State the blood parasite species.
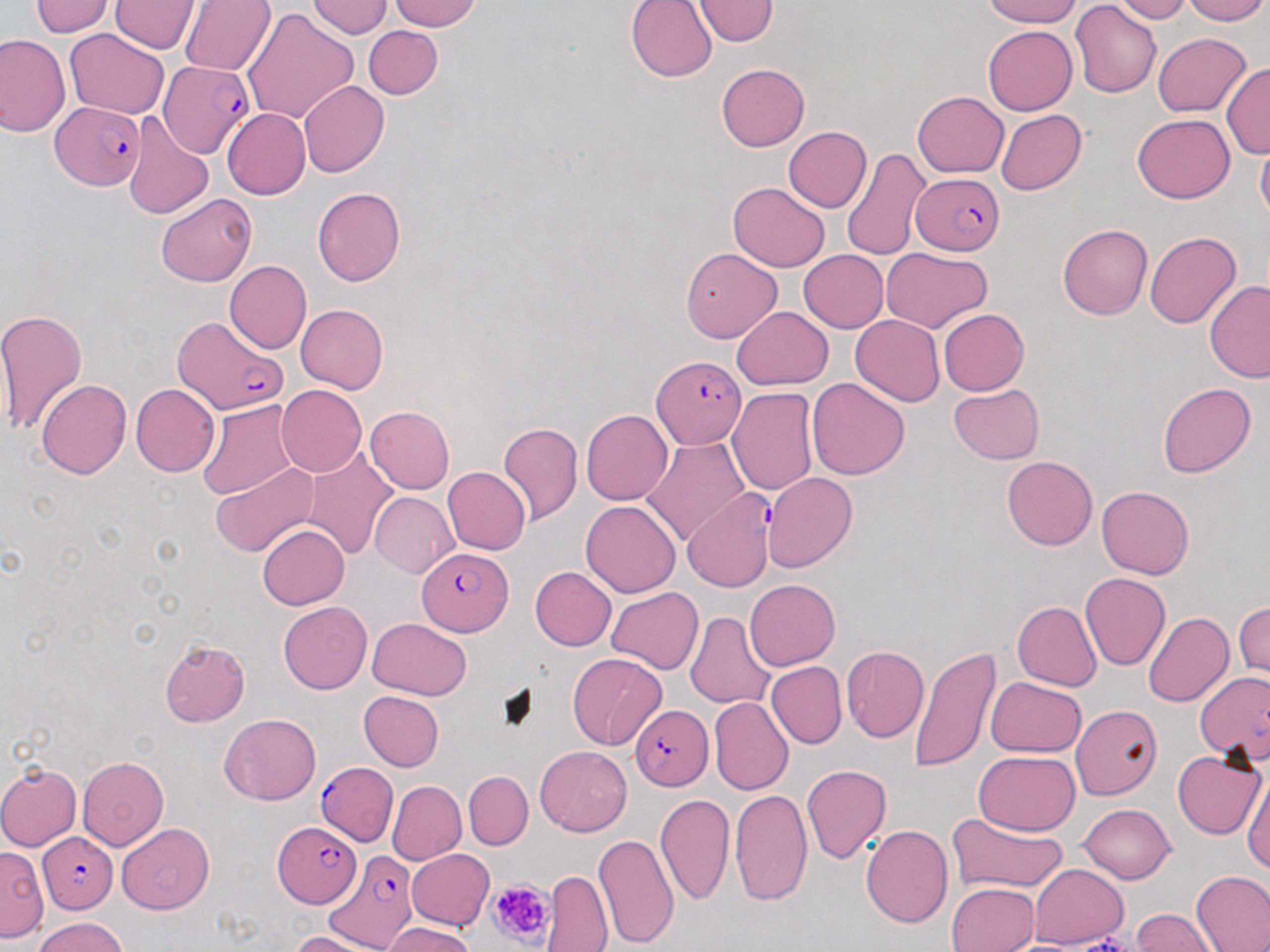

Plasmodium falciparum.

modality = optical microscopy
preparation = thin blood film
stain = May-Grünwald-Giemsa
image size = 1270×952 pixels
magnification = 1000x
platelet locations = approximate bounding boxes as (x1, y1, x2, y2) in pixels: (489, 877, 555, 947)
uninfected red blood cell locations = approximate bounding boxes as (x1, y1, x2, y2) in pixels: (306, 0, 393, 39), (386, 0, 483, 31), (626, 0, 718, 82), (692, 0, 779, 45), (982, 0, 1082, 27), (1180, 0, 1267, 25), (29, 1, 116, 37), (110, 1, 201, 54), (180, 1, 276, 76), (1110, 1, 1191, 23), (1070, 2, 1161, 99), (243, 7, 358, 125), (362, 25, 442, 99), (983, 25, 1076, 115), (64, 29, 169, 119), (1152, 33, 1251, 117), (0, 34, 70, 138), (1220, 62, 1270, 160), (717, 63, 809, 151), (299, 81, 390, 179), (912, 91, 1008, 177), (224, 97, 384, 187), (222, 109, 310, 199), (996, 110, 1087, 194), (121, 112, 214, 219), (1131, 114, 1236, 203), (784, 127, 872, 213), (1255, 136, 1270, 226), (842, 147, 932, 262), (728, 182, 830, 271), (312, 186, 405, 287), (156, 193, 257, 287), (1058, 224, 1152, 320), (1145, 232, 1242, 329), (681, 247, 781, 343), (882, 247, 991, 332), (799, 249, 889, 332), (224, 260, 311, 353), (1203, 280, 1270, 381), (295, 304, 388, 394), (732, 306, 832, 388), (0, 307, 88, 437), (939, 309, 1029, 396), (850, 315, 945, 406), (806, 378, 909, 480), (36, 379, 131, 480), (948, 383, 1044, 464), (1157, 383, 1256, 477), (131, 384, 220, 476), (277, 386, 366, 477), (727, 388, 818, 494), (197, 400, 300, 501), (365, 405, 454, 494), (581, 409, 672, 506), (497, 421, 583, 526), (642, 438, 749, 546), (299, 447, 399, 559), (1002, 456, 1098, 550), (210, 463, 318, 559), (442, 467, 531, 556), (764, 472, 857, 573), (1097, 487, 1194, 579), (370, 492, 460, 579), (580, 500, 681, 598), (258, 524, 350, 610), (529, 565, 617, 651), (1081, 572, 1171, 670), (743, 579, 840, 670), (606, 586, 703, 675), (278, 601, 371, 694), (1012, 601, 1102, 691), (1235, 601, 1269, 680), (685, 612, 776, 709), (1142, 612, 1234, 707), (367, 618, 472, 700), (160, 639, 251, 726), (909, 645, 1001, 773), (841, 646, 928, 742), (568, 652, 666, 749), (766, 661, 846, 749), (985, 677, 1087, 759), (359, 690, 444, 771), (709, 696, 793, 796), (1070, 706, 1162, 799), (219, 713, 322, 805), (534, 745, 631, 835), (1171, 749, 1266, 840), (973, 750, 1081, 834), (76, 756, 169, 851), (0, 763, 82, 851), (800, 764, 892, 864), (1242, 767, 1270, 874), (464, 771, 533, 850), (387, 781, 466, 865), (729, 788, 813, 905), (653, 792, 734, 906), (1078, 803, 1176, 884), (947, 811, 1068, 893), (116, 824, 215, 914), (861, 824, 954, 928), (593, 834, 678, 948), (0, 847, 48, 943), (406, 848, 494, 930), (1028, 865, 1128, 947), (1191, 869, 1270, 951), (543, 871, 612, 952), (947, 883, 1038, 951), (1131, 908, 1218, 951), (35, 917, 128, 952), (384, 922, 475, 952), (291, 931, 377, 951)
Plasmodium falciparum-infected red blood cell locations = approximate bounding boxes as (x1, y1, x2, y2) in pixels: (156, 60, 253, 158), (51, 101, 145, 190), (915, 171, 1006, 255), (172, 315, 287, 417), (651, 356, 748, 451), (682, 489, 776, 593), (418, 548, 511, 635), (1194, 672, 1270, 765), (630, 705, 714, 791), (316, 763, 397, 846), (272, 823, 359, 906), (37, 832, 117, 913), (327, 851, 416, 950)
field of view = one of a larger specimen